Locate and identify every blood parasite.
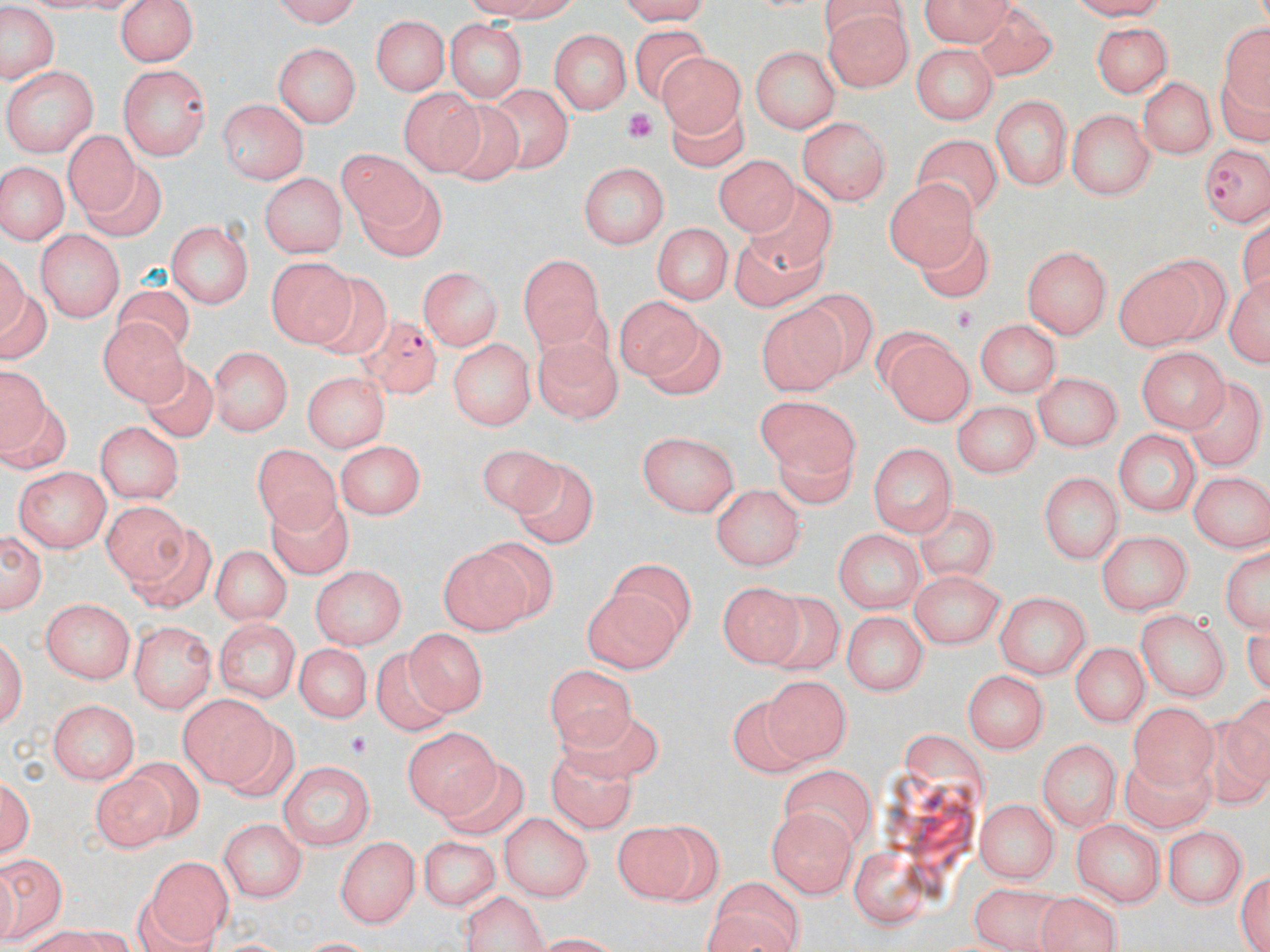
Approximate bounding boxes as (x1, y1, x2, y2) in pixels.
Plasmodium falciparum-infected red blood cells: (1201, 141, 1268, 230), (362, 316, 444, 405).
No Plasmodium ovale, Plasmodium malariae, Plasmodium vivax, Babesia divergens, or Trypanosoma brucei observed.

Uninfected red blood cell locations: (271, 0, 367, 25), (465, 0, 591, 27), (609, 0, 715, 23), (916, 0, 1016, 46), (112, 1, 197, 70), (826, 4, 912, 92), (1, 5, 58, 86), (977, 6, 1053, 79), (370, 14, 452, 97), (1213, 15, 1268, 148), (444, 18, 527, 105), (1087, 20, 1172, 99), (633, 26, 719, 104), (551, 29, 630, 113), (272, 41, 363, 129), (909, 42, 999, 123), (750, 43, 841, 136), (651, 48, 745, 146), (117, 64, 212, 158), (3, 66, 100, 154), (1134, 76, 1219, 160), (491, 86, 567, 174), (397, 88, 480, 173), (993, 95, 1071, 192), (219, 97, 310, 185), (673, 102, 749, 172), (436, 104, 526, 188), (1069, 107, 1158, 202), (800, 115, 890, 205), (63, 126, 138, 219), (914, 132, 1005, 217), (334, 147, 430, 233), (713, 149, 800, 237), (577, 161, 670, 248), (0, 163, 67, 244), (79, 165, 164, 240), (259, 171, 346, 257), (884, 178, 975, 272), (366, 180, 448, 263), (754, 187, 843, 271), (168, 220, 253, 308), (651, 223, 729, 305), (35, 228, 126, 321), (917, 230, 988, 304), (729, 237, 824, 312), (1025, 244, 1111, 339), (515, 253, 608, 348), (1111, 253, 1221, 351), (264, 254, 357, 345), (419, 266, 504, 352), (0, 267, 50, 362), (309, 275, 389, 359), (1223, 278, 1270, 370), (115, 279, 188, 358), (614, 293, 716, 391), (799, 293, 873, 370), (762, 308, 851, 399), (96, 317, 191, 409), (973, 318, 1062, 398), (873, 327, 975, 427), (534, 334, 619, 424), (449, 338, 534, 430), (208, 345, 291, 440), (1138, 348, 1225, 434), (139, 362, 220, 445), (0, 365, 48, 462), (304, 372, 391, 451), (1034, 374, 1126, 449), (1189, 383, 1262, 467), (954, 400, 1039, 478), (756, 402, 856, 478), (94, 423, 182, 506), (638, 428, 743, 515), (1115, 429, 1200, 517), (776, 436, 851, 506), (331, 441, 426, 518), (868, 441, 955, 541), (253, 443, 340, 531), (477, 445, 571, 523), (516, 464, 603, 548), (14, 466, 115, 552), (1038, 469, 1122, 562), (1188, 472, 1268, 553), (709, 482, 803, 571), (254, 494, 355, 577), (104, 507, 195, 594), (918, 508, 994, 585), (832, 525, 923, 612), (2, 528, 46, 616), (1096, 531, 1192, 616), (435, 541, 531, 635), (1217, 542, 1270, 638), (212, 544, 289, 626), (583, 562, 695, 671), (309, 567, 403, 647), (908, 569, 1003, 647), (717, 581, 798, 667), (994, 590, 1095, 676), (767, 594, 843, 675), (39, 598, 133, 682), (1135, 608, 1229, 701), (839, 610, 927, 697), (215, 619, 299, 704), (130, 620, 216, 711), (395, 626, 483, 716), (0, 629, 30, 741), (293, 646, 372, 728), (1072, 646, 1147, 726), (368, 651, 458, 732), (549, 660, 639, 752), (964, 667, 1047, 754), (765, 675, 847, 765), (182, 693, 274, 788), (48, 698, 140, 784), (1129, 699, 1215, 787), (723, 700, 815, 775), (554, 712, 668, 779), (219, 719, 297, 801), (1197, 720, 1270, 802), (401, 731, 499, 816), (1037, 737, 1119, 832), (552, 755, 633, 830), (1126, 758, 1214, 830), (92, 761, 184, 852), (278, 761, 374, 851), (436, 763, 523, 832), (782, 765, 874, 845), (2, 770, 37, 868), (974, 798, 1061, 883), (767, 807, 860, 898), (500, 812, 592, 903), (214, 817, 305, 905), (1070, 818, 1162, 904), (609, 819, 724, 904), (1163, 824, 1247, 910), (409, 831, 496, 917), (334, 833, 421, 929), (845, 841, 936, 928), (1, 849, 69, 943), (137, 855, 231, 949), (1234, 867, 1270, 952), (705, 878, 807, 952), (967, 888, 1065, 952), (1035, 891, 1123, 952), (464, 895, 545, 951), (23, 925, 146, 952). Platelet locations: (623, 109, 664, 144), (956, 307, 977, 331), (345, 733, 380, 758). Slide-level diagnosis: Plasmodium falciparum. Thin blood film. Single field of view. May-Grünwald-Giemsa stain. Light microscopy. 1000x magnification. Image is 1270×952 pixels.